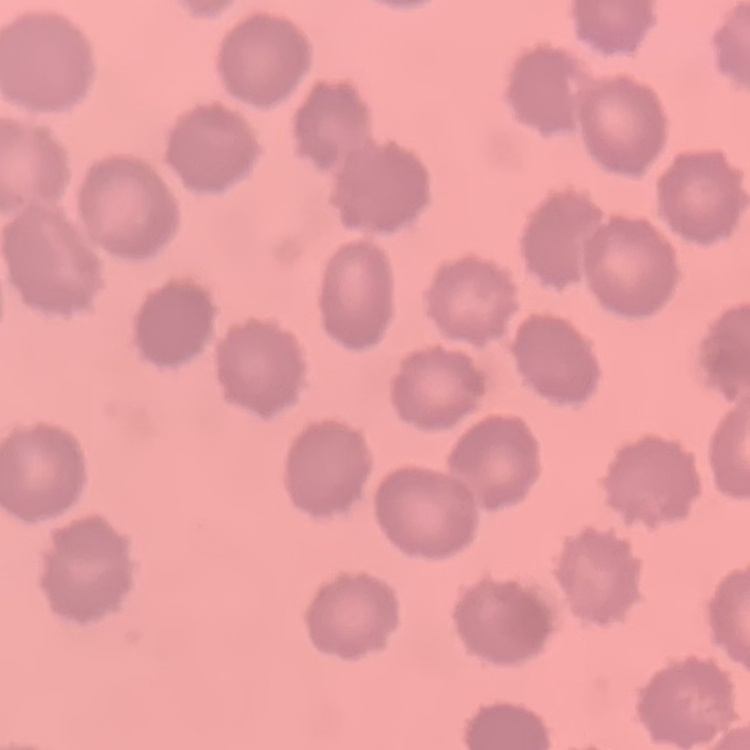
red blood cell morphology = no rouleaux formation
image type = square crop of a larger photomicrograph
stain = Field's or Giemsa
preparation = thin peripheral smear